State which parasite is depicted.
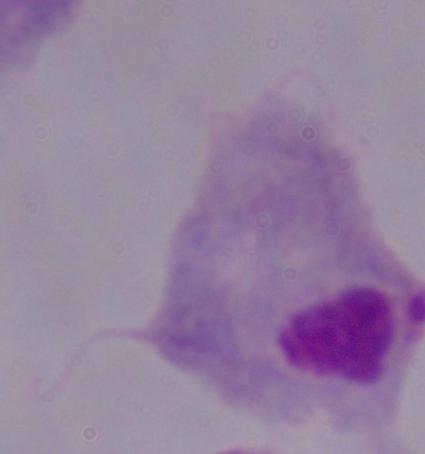
This is a trichomonad.

Summary:
  - Modality: photomicrograph
  - Magnification: 1000x